Assess this cell for malaria.
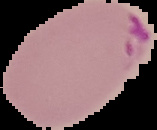

Parasitized.

image_size: 157×130 pixels
image_type: segmented cell region on a black background
preparation: thin blood smear